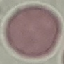
malaria status = uninfected
capture = smartphone camera at the microscope eyepiece
preparation = thin smear
stain = Giemsa
image type = automatically extracted cell patch, resized to 64 × 64 pixels